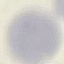

{
  "malaria_status": "uninfected",
  "preparation": "thin smear",
  "capture": "smartphone camera at the microscope eyepiece",
  "image_type": "cell patch, automatically extracted from a larger field of view and resized to 64 × 64 pixels",
  "stain": "Giemsa"
}